Assess this cell for malaria.
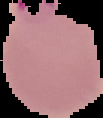

Parasitized.

image type = cell region segmented out of the field of view; surrounding area masked to black
image size = 103×118 pixels
preparation = thin blood smear